Identify the parasite.
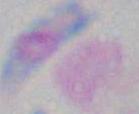

This is Toxoplasma gondii.

Captured at 1000x magnification. Micrograph.